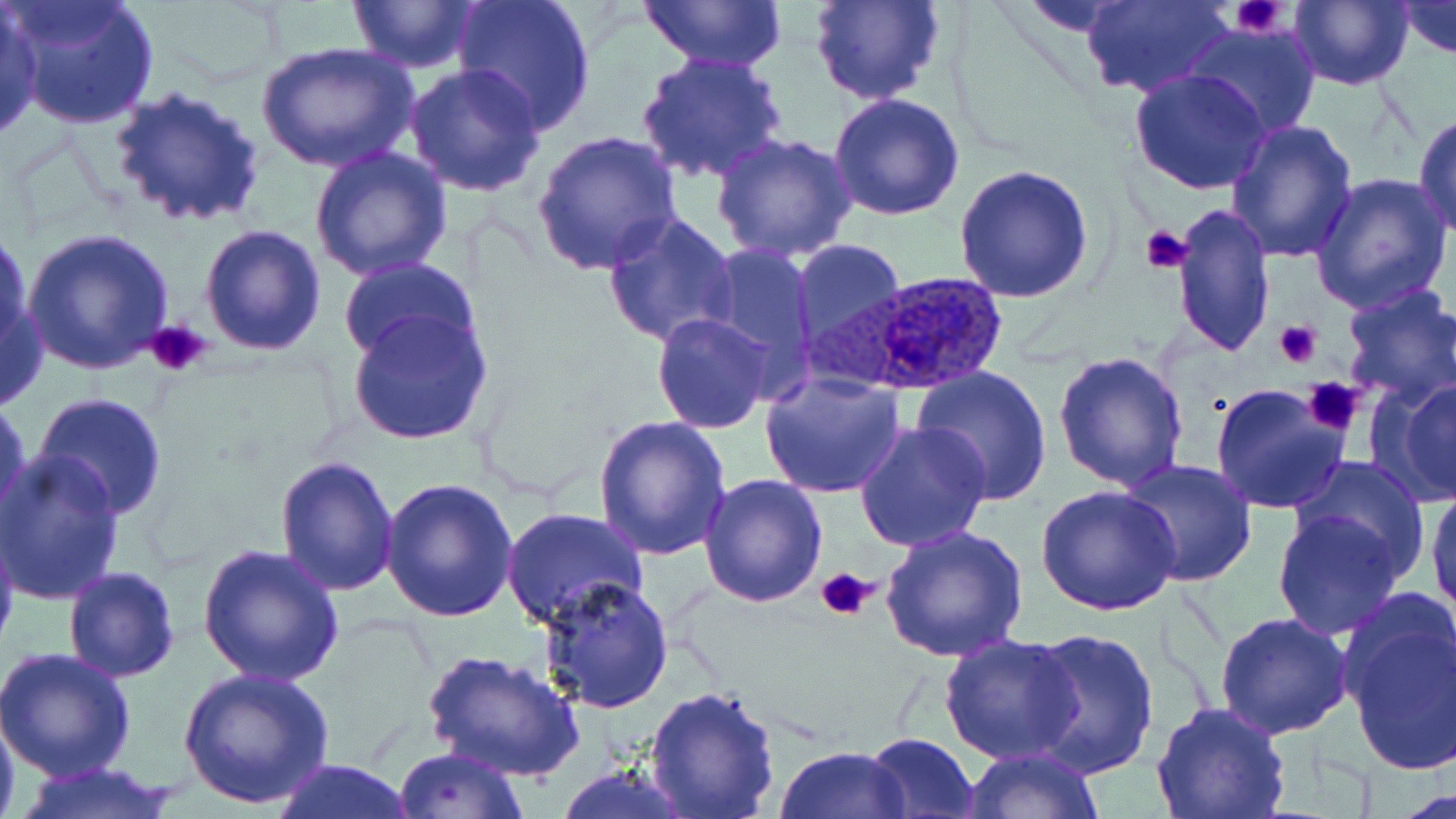

slide-level diagnosis = Plasmodium ovale
field of view = single
image size = 1456×819 pixels
Plasmodium ovale-infected red blood cell locations = approximate bounding boxes as (x1,y1)-(x2,y2) corner pairs in pixels: (791,270)-(1012,397)
modality = optical microscopy
magnification = 1000x
platelet locations = approximate bounding boxes as (x1,y1)-(x2,y2) corner pairs in pixels: (1231,0)-(1289,40), (1139,224)-(1192,275), (146,318)-(211,378), (1276,321)-(1321,370), (1304,378)-(1365,436), (815,566)-(875,622)
stain = May-Grünwald-Giemsa
preparation = thin blood smear
uninfected red blood cell locations = approximate bounding boxes as (x1,y1)-(x2,y2) corner pairs in pixels: (2,0)-(159,132), (450,0)-(597,134), (640,0)-(789,73), (810,0)-(948,106), (1081,0)-(1232,100), (1285,0)-(1413,90), (349,1)-(478,73), (1396,1)-(1456,59), (0,5)-(43,144), (1185,23)-(1322,138), (254,43)-(419,175), (635,51)-(790,185), (404,62)-(549,196), (1129,69)-(1274,196), (111,86)-(266,230), (829,93)-(964,221), (1412,112)-(1456,238), (1226,119)-(1359,263), (529,128)-(681,276), (712,133)-(857,263), (311,146)-(451,283), (952,163)-(1097,304), (1309,171)-(1453,315), (1172,202)-(1275,358), (602,211)-(740,349), (199,224)-(328,357), (0,226)-(33,369), (21,230)-(175,378), (790,241)-(906,354), (698,242)-(820,393), (336,257)-(483,368), (0,265)-(47,415), (1337,283)-(1456,413), (349,308)-(492,446), (651,313)-(774,433), (1052,350)-(1189,493), (912,366)-(1056,506), (759,372)-(906,500), (1384,378)-(1456,505), (1209,383)-(1349,514), (35,392)-(168,518), (0,394)-(32,531), (592,416)-(734,561), (854,421)-(993,554), (1,453)-(126,605), (275,455)-(400,597), (1291,455)-(1432,578), (1119,459)-(1257,586), (698,473)-(828,609), (378,477)-(517,621), (1426,480)-(1456,620), (1035,485)-(1181,616), (501,507)-(647,629), (1272,507)-(1405,638), (0,514)-(21,661), (880,525)-(1029,664), (200,544)-(342,687), (62,566)-(180,681), (537,578)-(674,713), (1342,604)-(1456,778), (1213,611)-(1354,739), (1022,627)-(1161,780), (937,632)-(1083,765), (0,646)-(135,782), (423,649)-(585,782), (177,667)-(335,808), (644,685)-(782,819), (1150,701)-(1292,819), (0,706)-(20,819), (863,732)-(980,819), (392,744)-(529,818), (774,744)-(911,818), (961,746)-(1103,819), (268,758)-(417,818), (554,763)-(698,819), (9,764)-(186,819)